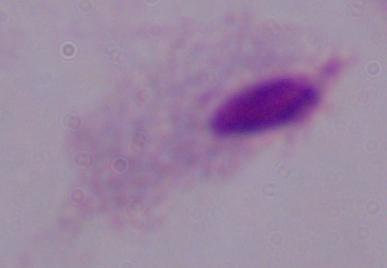
Summary:
  - Identification: trichomonad
  - Modality: micrograph
  - Magnification: 1000x